Report the malaria status of this cell.
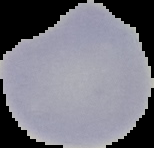
It is uninfected.

The area outside the segmented cell region is set to black. From a thin blood film. Image is 154×148 pixels.